Comment on the morphology of the erythrocytes.
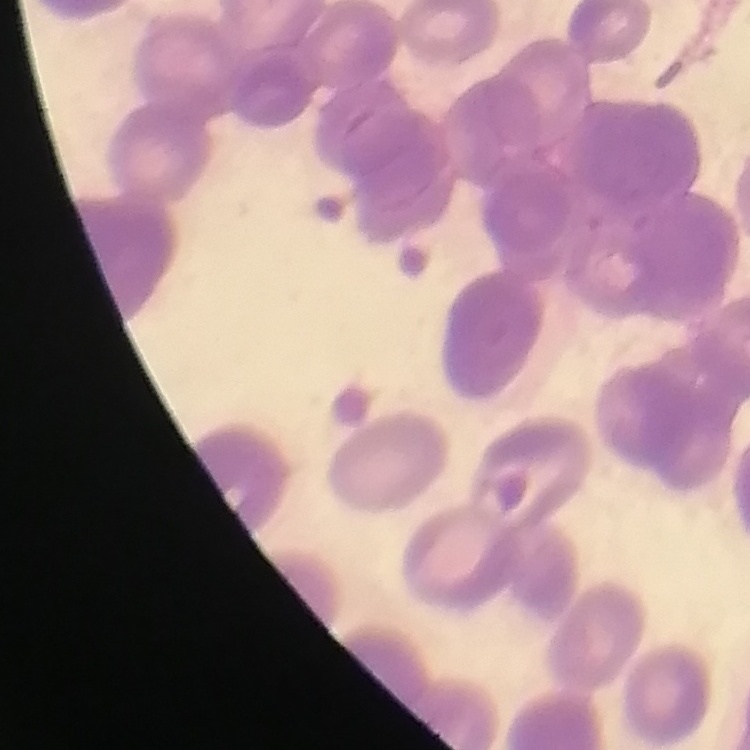
They show rouleaux formation.

preparation = thin peripheral smear
image type = square crop of a larger photomicrograph
stain = Field's or Giemsa